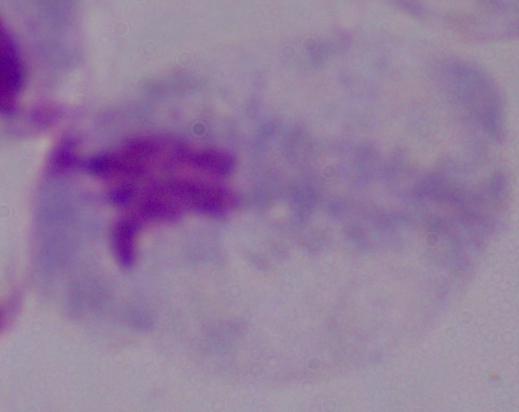
Summary:
  - Magnification: 1000x
  - Modality: micrograph
  - Identification: trichomonad